Outline each blood parasite and name the species.
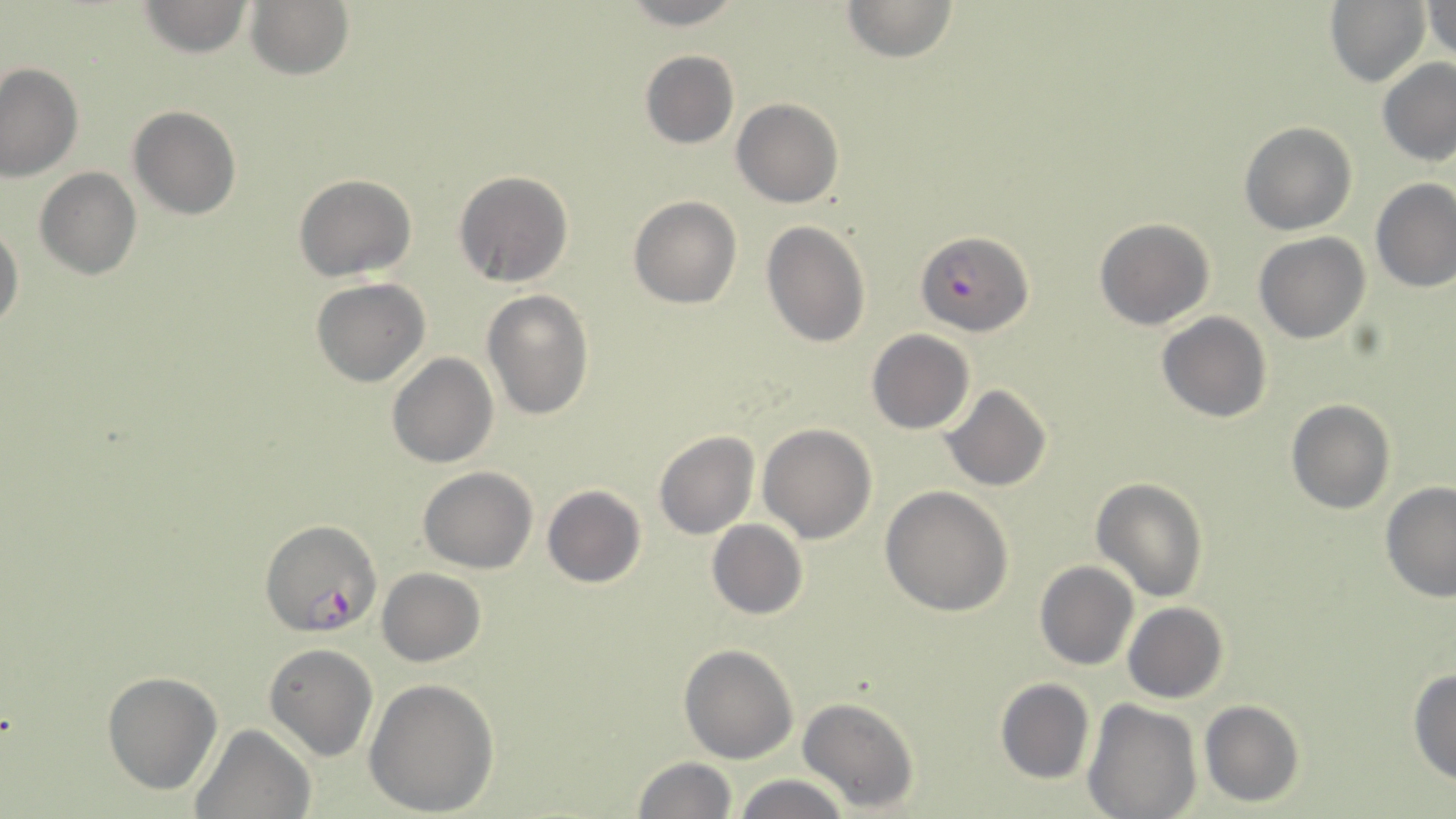

Approximate bounding boxes as (x1,y1)-(x2,y2) corner pairs in pixels.
Plasmodium falciparum-infected red blood cells: (916,231)-(1032,336), (261,519)-(378,638).
No Plasmodium ovale, Plasmodium malariae, Plasmodium vivax, Babesia divergens, or Trypanosoma brucei observed.

Summary:
  - Uninfected red blood cell locations: (136,0)-(256,57), (621,0)-(746,28), (841,0)-(960,63), (1325,0)-(1431,88), (1425,1)-(1455,61), (245,2)-(354,80), (639,50)-(739,150), (1377,57)-(1456,165), (0,64)-(83,183), (732,99)-(842,207), (129,105)-(241,220), (1240,122)-(1357,235), (34,168)-(141,279), (453,169)-(575,286), (294,174)-(415,281), (1371,178)-(1455,293), (627,196)-(742,309), (1095,218)-(1215,331), (761,221)-(871,349), (0,223)-(24,334), (1254,233)-(1370,343), (311,278)-(430,386), (482,287)-(595,421), (1157,311)-(1272,422), (867,329)-(973,434), (387,352)-(498,469), (942,385)-(1052,491), (1285,398)-(1395,514), (758,424)-(877,543), (652,431)-(759,539), (417,465)-(538,574), (1091,478)-(1209,603), (1378,482)-(1456,601), (542,485)-(647,588), (881,486)-(1014,616), (706,520)-(808,620), (1035,561)-(1139,670), (377,568)-(484,667), (1123,602)-(1229,703), (679,643)-(799,765), (263,644)-(379,763), (1409,667)-(1456,787), (101,671)-(223,794), (363,678)-(498,816), (994,679)-(1095,784), (797,696)-(920,811), (1083,699)-(1203,819), (1199,700)-(1305,806), (190,723)-(312,819), (631,756)-(739,818), (733,774)-(854,819)
  - Slide-level diagnosis: Plasmodium falciparum
  - Preparation: thin blood smear
  - Stain: May-Grünwald-Giemsa
  - Field of view: single
  - Image size: 1456×819 pixels
  - Magnification: 1000x
  - Modality: optical microscopy